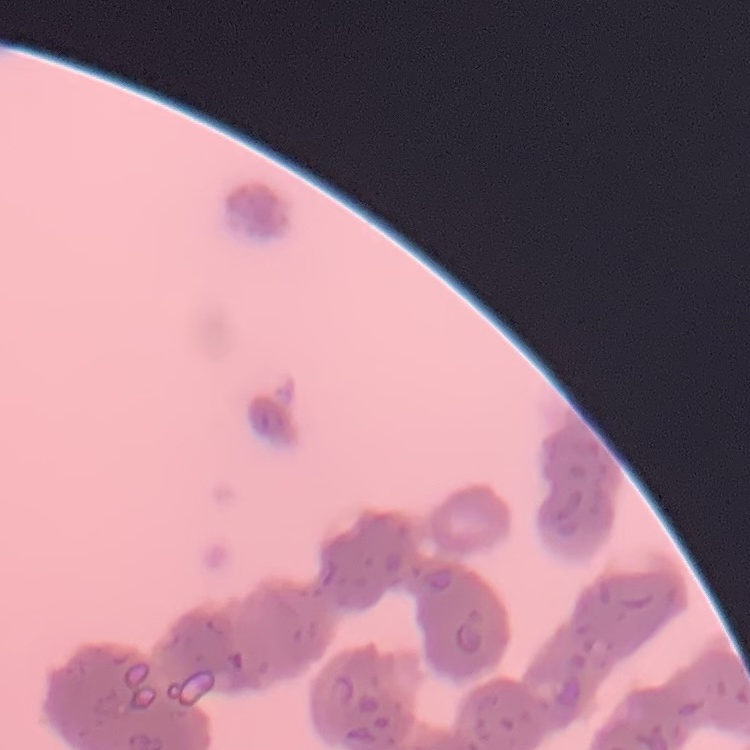
The red blood cells show rouleaux formation. Field's or Giemsa stain. Thin blood film. Square crop of a larger photomicrograph.